Outline each Plasmodium falciparum-infected red blood cell.
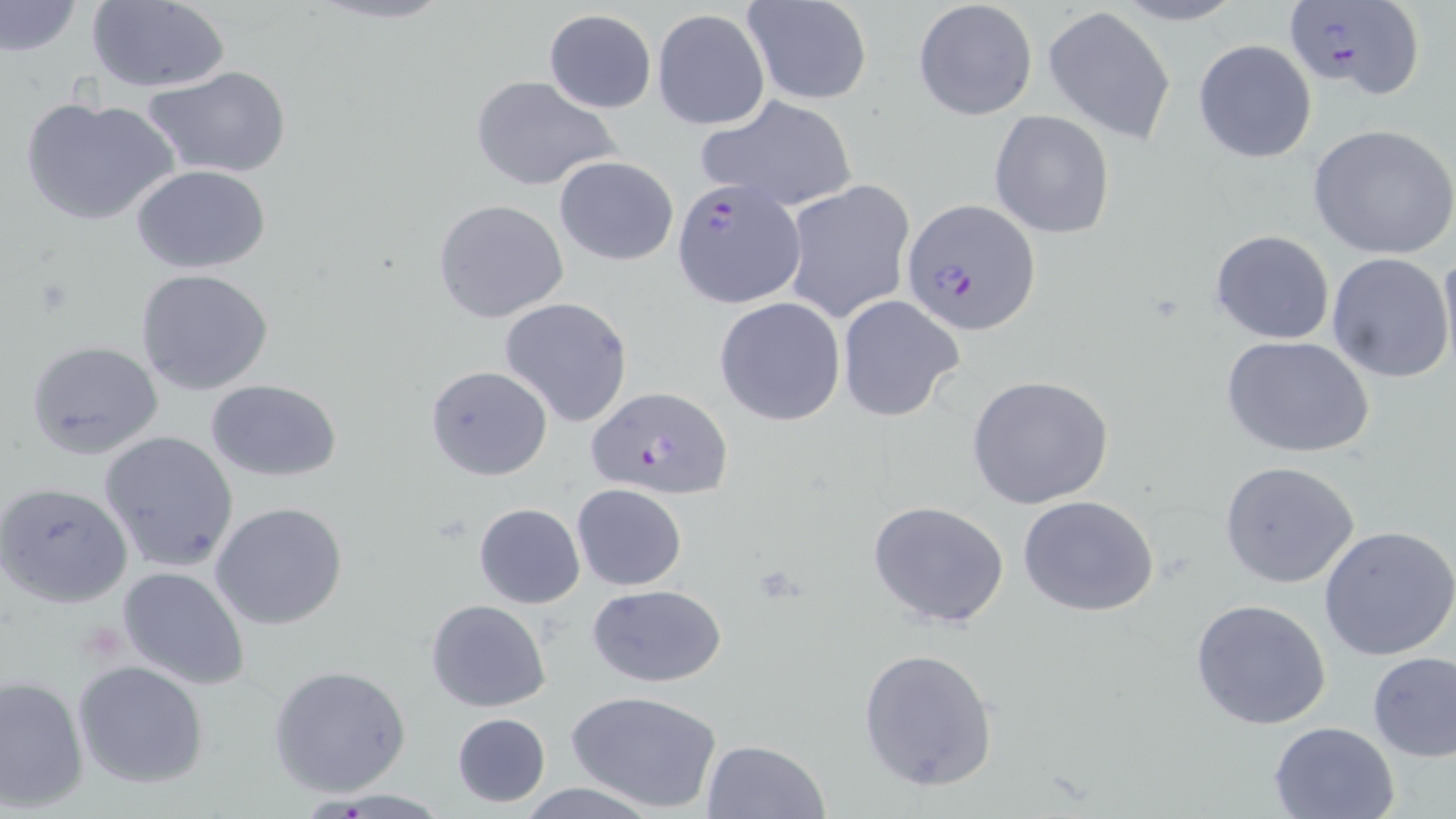

Approximate bounding boxes as [x1, y1, x2, y2] in pixels.
Plasmodium falciparum-infected red blood cells: [1285, 1, 1425, 101], [670, 176, 805, 320], [901, 200, 1041, 336], [587, 385, 734, 499].

Summary:
  - Uninfected red blood cell locations: [306, 0, 458, 26], [744, 0, 872, 105], [0, 1, 81, 56], [84, 1, 231, 92], [913, 2, 1036, 120], [1044, 6, 1176, 145], [543, 9, 656, 113], [652, 9, 770, 131], [1193, 39, 1317, 164], [143, 64, 292, 180], [468, 74, 623, 192], [21, 94, 180, 228], [695, 94, 859, 213], [988, 110, 1115, 240], [1306, 124, 1456, 259], [554, 156, 679, 267], [133, 165, 272, 275], [782, 179, 915, 325], [433, 198, 569, 323], [1210, 229, 1335, 344], [1437, 247, 1456, 377], [1326, 253, 1455, 382], [135, 268, 275, 395], [836, 294, 964, 422], [714, 296, 846, 427], [499, 297, 634, 428], [1222, 335, 1376, 459], [26, 342, 165, 461], [425, 364, 553, 480], [966, 375, 1115, 509], [206, 379, 342, 482], [99, 430, 238, 573], [1219, 460, 1361, 589], [1, 482, 133, 607], [571, 483, 688, 591], [1017, 493, 1160, 617], [211, 500, 347, 629], [867, 500, 1010, 629], [473, 503, 585, 607], [1318, 525, 1456, 662], [117, 562, 251, 691], [587, 585, 729, 687], [1190, 598, 1333, 730], [427, 599, 550, 712], [856, 646, 998, 792], [1366, 650, 1456, 763], [73, 660, 209, 789], [269, 664, 412, 798], [1, 675, 89, 811], [566, 688, 722, 814], [451, 712, 551, 806], [1267, 720, 1399, 818], [701, 739, 831, 819], [513, 782, 666, 819], [302, 788, 454, 816]
  - Slide-level diagnosis: Plasmodium falciparum
  - Modality: light microscopy
  - Image size: 1456×819 pixels
  - Stain: May-Grünwald-Giemsa
  - Preparation: thin blood film
  - Field of view: one of a larger specimen
  - Magnification: 1000x